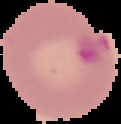
malaria status = parasitized
preparation = thin blood smear
image type = cell region segmented out of the field of view; surrounding area masked to black
image size = 121×124 pixels